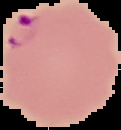
Result: Plasmodium parasites identified. Segmented cell region on a black background. From a thin blood smear. Image is 121×130 pixels.